Report the malaria status of this cell.
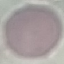

Uninfected.

stain = Giemsa
image type = automatically extracted cell patch, resized to 64 × 64 pixels
preparation = thin blood smear
capture = smartphone through the microscope eyepiece